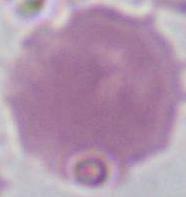

Summary:
  - Identification: erythrocyte
  - Magnification: 1000x
  - Modality: photomicrograph